Assess this cell for malaria.
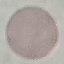

It is uninfected.

Automatically extracted cell patch, resized to 64 × 64 pixels. Thin smear of blood. Giemsa-stained preparation. Photographed with a smartphone camera at the microscope eyepiece.